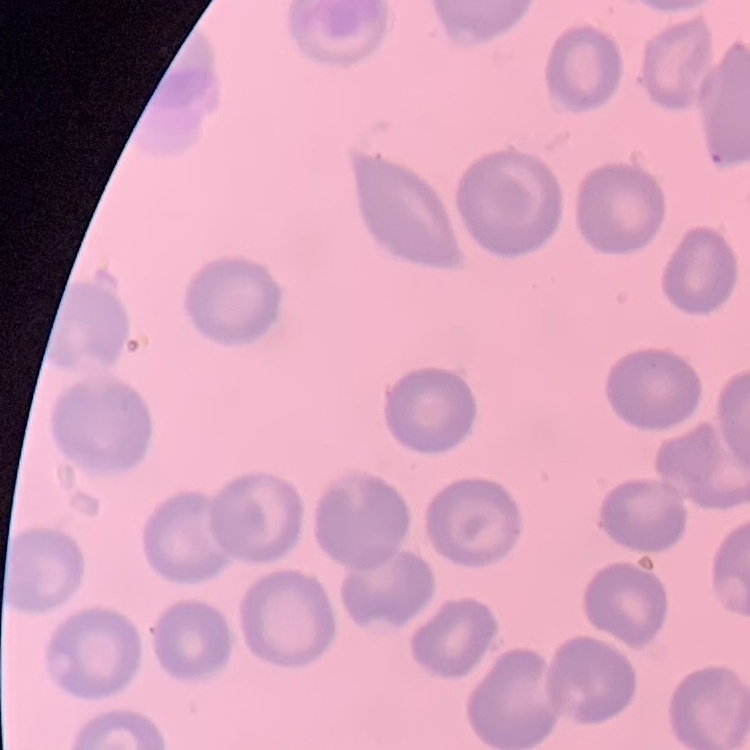
The erythrocytes exhibit no rouleaux formation. Thin peripheral smear. Stained with either Field's or Giemsa. One tile cut from a larger photomicrograph.